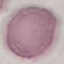 Result: no malaria parasites detected. Giemsa stain. Thin blood smear. Photographed with a smartphone camera at the microscope eyepiece. Automatically extracted cell patch, resized to 64 × 64 pixels.